Assess this cell for malaria.
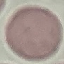
It is uninfected.

Summary:
  - Preparation: thin blood smear
  - Capture: smartphone through the microscope eyepiece
  - Stain: Giemsa
  - Image type: cell patch, automatically extracted from a larger field of view and resized to 64 × 64 pixels